Give the position of every leukocyte visible.
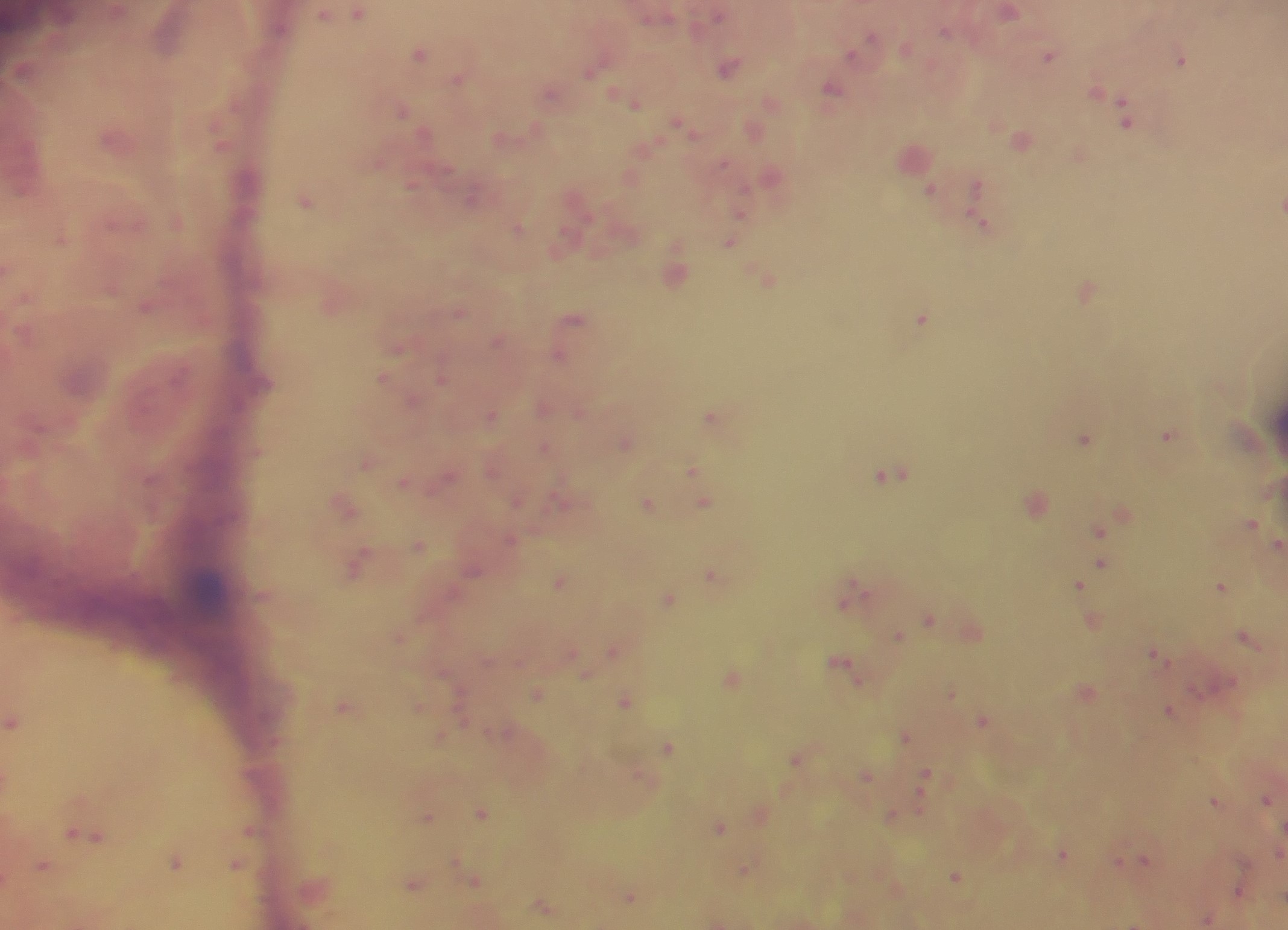

No leukocytes observed.

preparation: thick blood smear
plasmodium_parasite_locations: 'approximate centers as {x, y} in pixels: {358, 12}, {1008, 12}, {341, 13}, {168, 33}, {867, 44}, {420, 53}, {1049, 55}, {1182, 59}, {729, 67}, {23, 70}, {459, 78}, {832, 89}, {552, 92}, {1098, 93}, {629, 100}, {771, 102}, {402, 109}, {1126, 114}, {684, 125}, {754, 129}, {424, 133}, {513, 136}, {116, 137}, {1022, 139}, {221, 142}, {914, 156}, {771, 175}, {631, 177}, {413, 183}, {977, 185}, {931, 191}, {473, 200}, {306, 201}, {1280, 206}, {740, 213}, {177, 220}, {983, 221}, {518, 228}, {62, 237}, {731, 242}, {9, 268}, {677, 270}, {767, 278}, {1086, 288}, {333, 302}, {148, 305}, {459, 312}, {574, 317}, {921, 317}, {568, 333}, {499, 339}, {559, 354}, {384, 377}, {442, 377}, {414, 400}, {543, 406}, {491, 415}, {712, 416}, {1169, 434}, {1085, 438}, {626, 442}, {545, 447}, {368, 462}, {494, 468}, {692, 470}, {891, 473}, {446, 478}, {406, 481}, {697, 481}, {561, 500}, {517, 501}, {1036, 501}, {704, 503}, {345, 504}, {648, 504}, {1122, 511}, {1252, 523}, {1100, 531}, {511, 540}, {1277, 543}, {419, 545}, {357, 563}, {1100, 566}, {473, 570}, {713, 573}, {1089, 574}, {560, 581}, {1080, 584}, {1222, 587}, {851, 597}, {669, 598}, {929, 619}, {1092, 621}, {972, 631}, {400, 637}, {899, 637}, {1249, 639}, {614, 649}, {1156, 654}, {844, 664}, {585, 673}, {732, 678}, {1086, 690}, {952, 692}, {537, 693}, {626, 702}, {345, 706}, {419, 708}, {1170, 710}, {985, 720}, {14, 721}, {906, 735}, {442, 737}, {669, 747}, {797, 758}, {867, 774}, {926, 777}, {1268, 798}, {1216, 800}, {482, 813}, {760, 814}, {428, 816}, {894, 816}, {720, 827}, {252, 830}, {86, 834}, {1280, 853}, {1063, 854}, {1145, 861}, {176, 863}, {1126, 863}, {237, 865}, {44, 867}, {746, 870}, {956, 876}, {474, 878}, {414, 883}, {315, 885}, {896, 888}, {1240, 891}, {630, 896}, {543, 905}, {1208, 918}'
field_of_view: single
image_size: 1288×930 pixels
country: Ghana
capture: mobile-phone photograph through a microscope